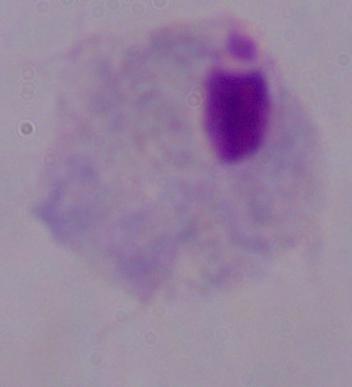

Summary:
  - Identification: trichomonad
  - Magnification: 1000x
  - Modality: photomicrograph